Locate and identify every blood parasite.
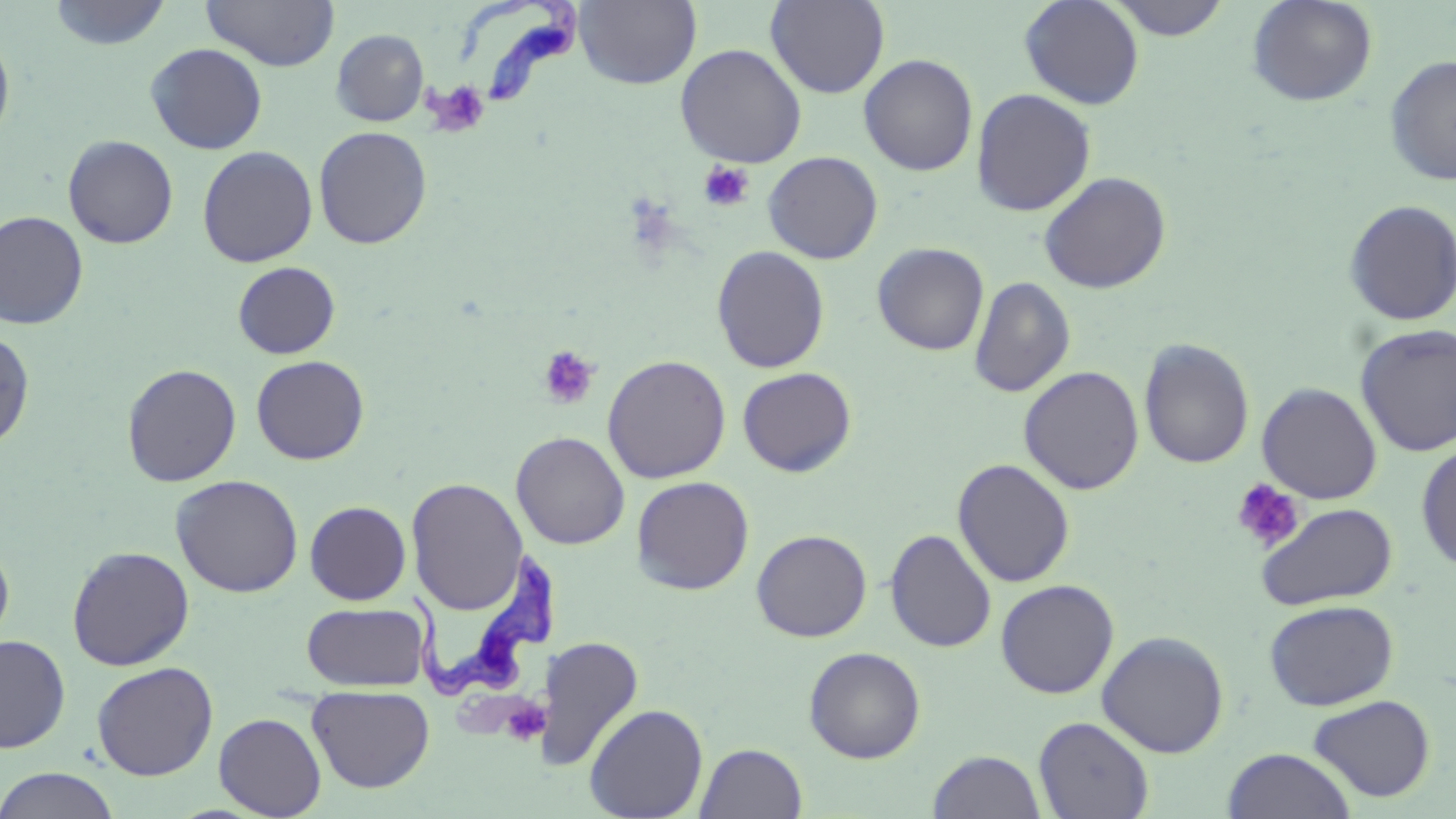

Approximate bounding boxes as [x1, y1, x2, y2] in pixels.
Trypanosoma brucei: [450, 2, 581, 107], [399, 537, 558, 704].
No Plasmodium falciparum, Plasmodium ovale, Plasmodium malariae, Plasmodium vivax, or Babesia divergens observed.

Uninfected red blood cell locations: [49, 0, 171, 50], [203, 0, 339, 71], [574, 0, 702, 89], [766, 0, 889, 97], [1018, 0, 1145, 110], [1107, 0, 1232, 41], [1246, 0, 1378, 107], [331, 29, 429, 126], [0, 32, 15, 147], [145, 43, 267, 154], [675, 43, 807, 168], [858, 53, 979, 176], [1384, 54, 1456, 187], [971, 88, 1096, 216], [313, 126, 432, 249], [63, 134, 178, 249], [197, 145, 318, 267], [762, 151, 883, 264], [1039, 171, 1172, 294], [1343, 200, 1456, 326], [0, 210, 88, 329], [872, 242, 989, 355], [711, 245, 830, 373], [232, 261, 341, 359], [969, 276, 1076, 398], [1354, 324, 1456, 457], [0, 329, 35, 451], [1139, 338, 1254, 469], [251, 354, 370, 465], [602, 354, 731, 483], [121, 363, 241, 487], [1018, 365, 1144, 494], [737, 367, 857, 478], [1257, 382, 1382, 504], [510, 430, 630, 549], [1416, 442, 1456, 573], [953, 458, 1075, 587], [170, 475, 304, 598], [631, 475, 754, 595], [406, 477, 528, 615], [304, 501, 411, 605], [1256, 503, 1398, 610], [885, 528, 997, 653], [751, 530, 872, 642], [0, 537, 15, 658], [67, 545, 195, 671], [995, 579, 1119, 699], [1263, 599, 1398, 710], [301, 602, 430, 692], [1096, 630, 1230, 757], [0, 634, 71, 753], [538, 636, 644, 772], [804, 646, 926, 763], [91, 662, 218, 780], [307, 685, 435, 793], [1308, 694, 1435, 802], [584, 703, 709, 819], [214, 712, 326, 818], [1034, 716, 1155, 819], [695, 743, 807, 819], [1222, 748, 1357, 819], [927, 750, 1046, 818], [0, 767, 122, 819]. Platelet locations: [424, 80, 491, 136], [698, 161, 756, 212], [536, 345, 601, 410], [1231, 478, 1303, 553], [503, 694, 553, 744]. Slide-level diagnosis: Trypanosoma brucei. Thin blood smear. 1000x magnification. Image is 1456×819 pixels. Light microscopy. Single field of view. May-Grünwald-Giemsa-stained preparation.